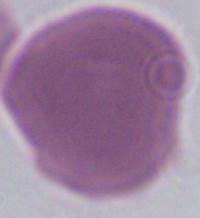

modality = micrograph
identification = erythrocyte
magnification = 1000x